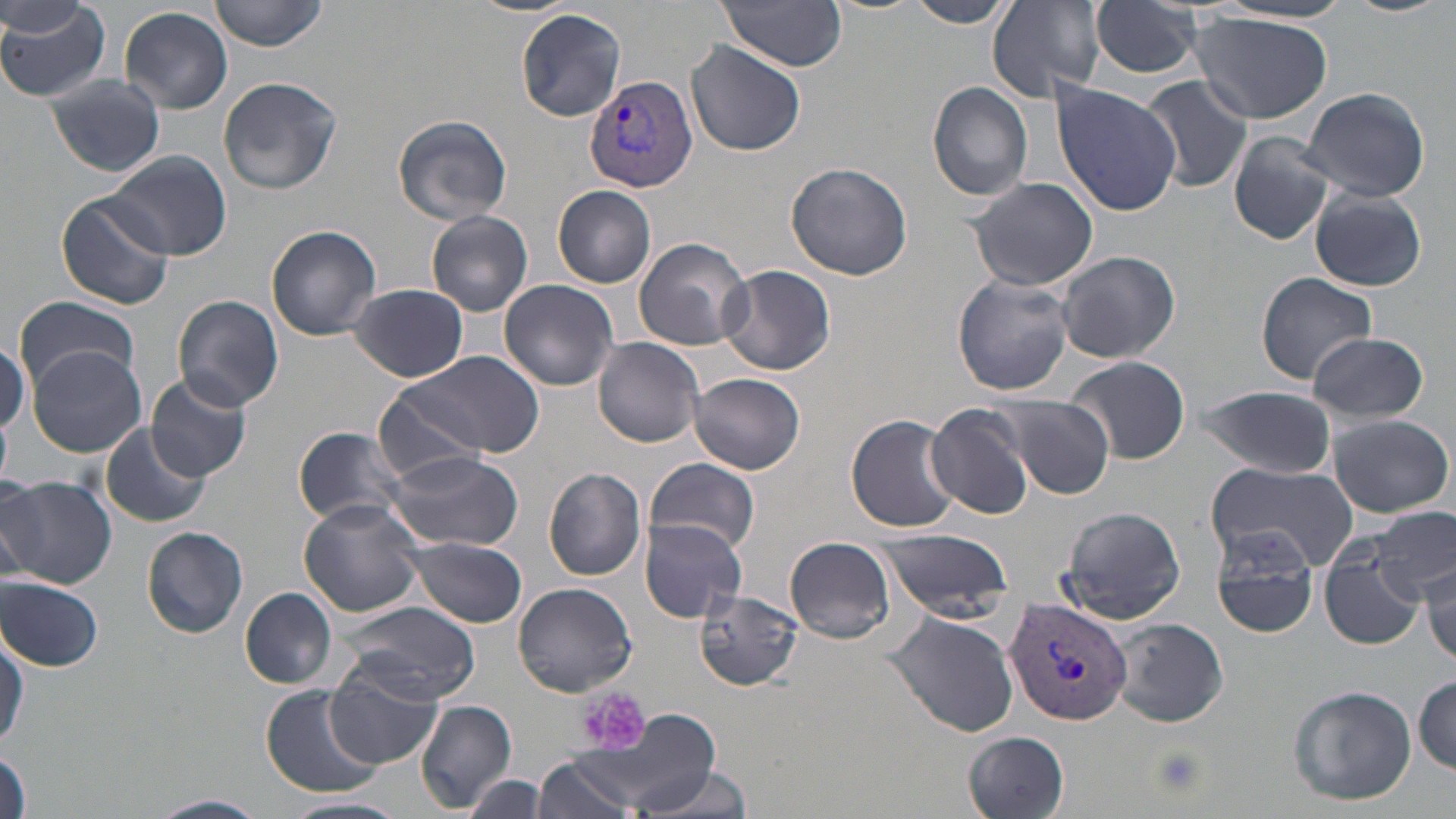

Approximate bounding boxes as (x1, y1, x2, y2) in pixels. Uninfected red blood cell locations: (0, 0, 111, 102), (208, 0, 327, 52), (465, 0, 580, 17), (719, 0, 848, 70), (987, 0, 1107, 103), (1089, 0, 1205, 79), (1338, 0, 1453, 17), (908, 1, 1011, 29), (1213, 1, 1356, 25), (120, 6, 233, 113), (516, 8, 626, 122), (1190, 14, 1332, 123), (686, 40, 806, 157), (47, 75, 167, 178), (1138, 75, 1252, 193), (218, 76, 343, 196), (928, 81, 1033, 202), (1050, 81, 1183, 216), (1303, 85, 1431, 202), (391, 113, 513, 226), (1228, 130, 1338, 246), (106, 152, 230, 260), (784, 161, 913, 280), (965, 176, 1099, 291), (553, 185, 657, 288), (1310, 189, 1427, 292), (56, 192, 177, 311), (426, 209, 533, 316), (266, 225, 382, 340), (633, 236, 752, 351), (1056, 249, 1181, 364), (719, 264, 836, 376), (1255, 272, 1375, 385), (951, 275, 1074, 398), (499, 278, 619, 390), (348, 283, 469, 382), (174, 295, 283, 412), (12, 298, 141, 386), (1308, 331, 1430, 423), (595, 336, 706, 448), (0, 343, 29, 436), (26, 345, 147, 458), (392, 351, 543, 459), (1064, 356, 1192, 465), (145, 372, 252, 481), (689, 372, 806, 473), (1195, 384, 1338, 479), (373, 386, 491, 485), (985, 395, 1115, 496), (927, 404, 1035, 520), (1, 410, 12, 488), (1327, 413, 1453, 518), (847, 414, 959, 531), (99, 422, 211, 528), (294, 426, 410, 528), (387, 449, 524, 552), (646, 457, 760, 556), (1204, 460, 1358, 572), (543, 468, 646, 580), (1, 476, 117, 588), (0, 477, 44, 588), (298, 498, 425, 618), (1057, 506, 1188, 624), (1369, 508, 1455, 590), (639, 518, 748, 622), (142, 526, 249, 639), (874, 528, 1016, 620), (1208, 529, 1322, 639), (785, 537, 896, 644), (400, 538, 528, 626), (1318, 551, 1427, 651), (1417, 555, 1454, 667), (1, 576, 104, 671), (513, 583, 636, 694), (239, 587, 337, 688), (694, 589, 802, 691), (341, 600, 481, 705), (882, 612, 1021, 737), (1108, 617, 1229, 729), (0, 642, 24, 744), (325, 668, 441, 769), (1412, 676, 1455, 774), (260, 684, 381, 798), (1286, 685, 1416, 807), (416, 699, 517, 812), (580, 708, 726, 817), (964, 732, 1071, 819), (1, 749, 31, 819), (534, 754, 639, 819), (630, 764, 755, 819), (462, 773, 548, 819), (150, 793, 268, 818), (280, 796, 407, 819). Platelet locations: (578, 687, 652, 753), (1148, 745, 1208, 799). Plasmodium vivax-infected red blood cell locations: (585, 74, 697, 193), (1003, 597, 1132, 723). Slide-level diagnosis: Plasmodium vivax. Optical microscopy. 1000x magnification. Image is 1456×819 pixels. Single field of view. Thin blood smear. May-Grünwald-Giemsa stain.